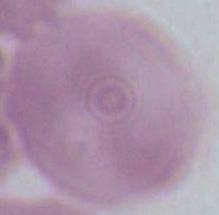
Summary:
  - Modality: photomicrograph
  - Identification: erythrocyte
  - Magnification: 1000x